Locate the Plasmodium falciparum-infected red blood cells and any of indeterminate infection status.
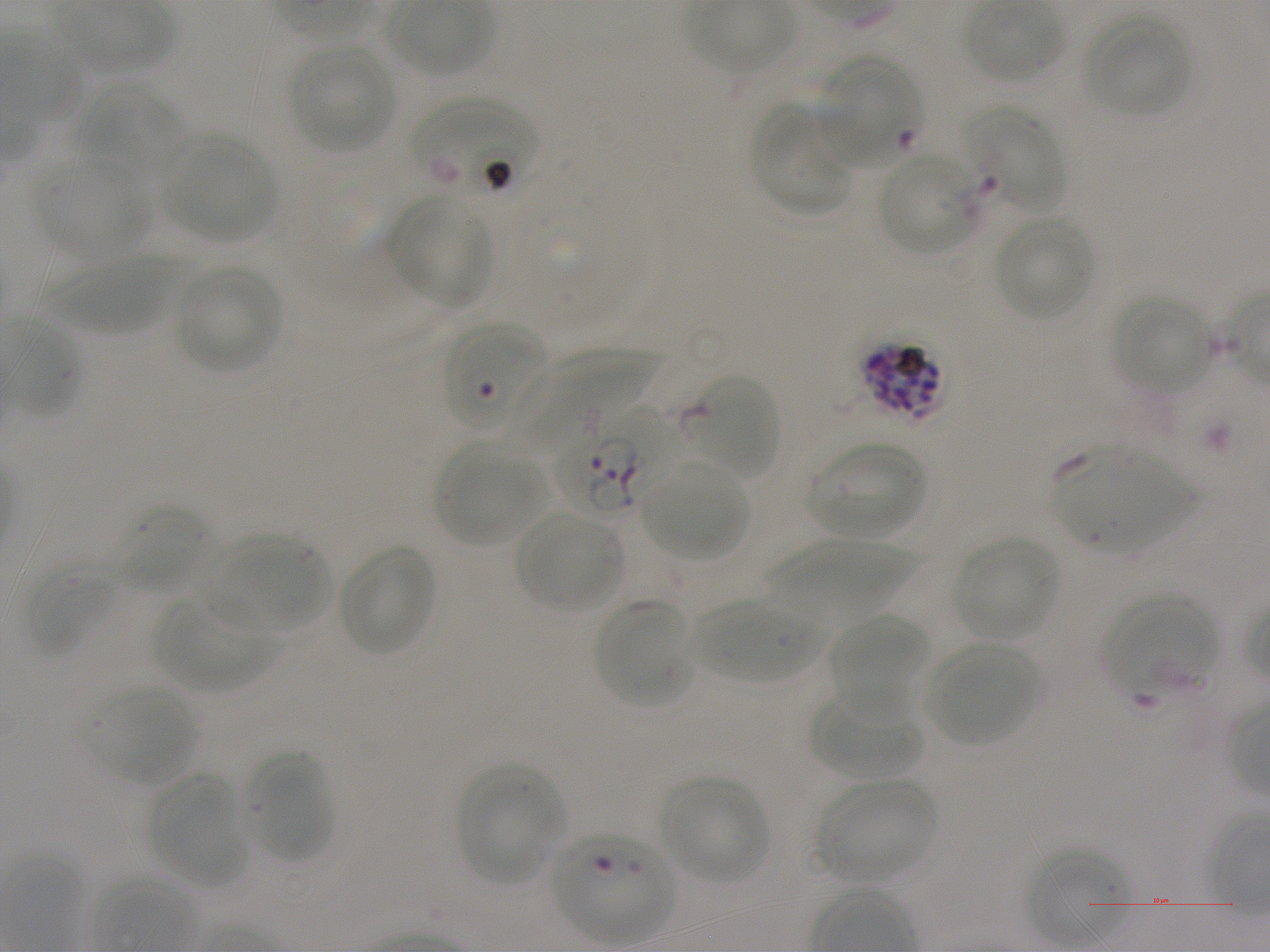
Approximate bounding boxes as (x1, y1, x2, y2) in pixels. Not every red blood cell is marked. A life-cycle stage — or a range of stages, where the recorded stages span more than one — follows each staged infected red blood cell.
Infected red blood cells: (820, 57, 920, 168) early ring; (859, 340, 945, 420); (558, 408, 680, 517).
Red blood cells of indeterminate infection status: (414, 97, 537, 200), (443, 323, 545, 431), (552, 833, 674, 943).

locations of uninfected red blood cells = (965, 1, 1064, 83), (1083, 14, 1192, 118), (289, 44, 396, 153), (68, 83, 181, 186), (751, 105, 849, 214), (964, 106, 1066, 213), (164, 132, 277, 242), (877, 151, 978, 257), (35, 157, 149, 258), (387, 195, 495, 310), (995, 215, 1095, 320), (46, 254, 186, 334), (174, 265, 282, 373), (1112, 293, 1212, 393), (510, 350, 653, 449), (682, 374, 780, 479), (806, 441, 926, 539), (434, 445, 546, 546), (1058, 446, 1190, 551), (641, 463, 747, 559), (115, 506, 216, 595), (513, 509, 623, 613), (213, 534, 328, 634), (952, 536, 1059, 641), (766, 540, 914, 617), (337, 544, 436, 656), (23, 564, 120, 657), (153, 595, 276, 692), (1106, 595, 1216, 700), (693, 597, 826, 684), (594, 600, 694, 709), (827, 613, 930, 716), (926, 642, 1039, 747), (86, 686, 196, 786), (812, 690, 921, 778), (244, 750, 332, 862), (456, 764, 562, 884), (147, 776, 245, 886), (659, 777, 768, 885), (816, 779, 937, 884), (1027, 849, 1127, 948)
preparation = thin blood film
objective = 100x, oil immersion, numerical aperture 1.25
culture = Plasmodium falciparum strain NF54, static, in vitro
donor blood group = A+
field of view = single
stain = Giemsa
image size = 1270×952 pixels